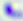
modality: micrograph
magnification: 400x
identification: Toxoplasma gondii